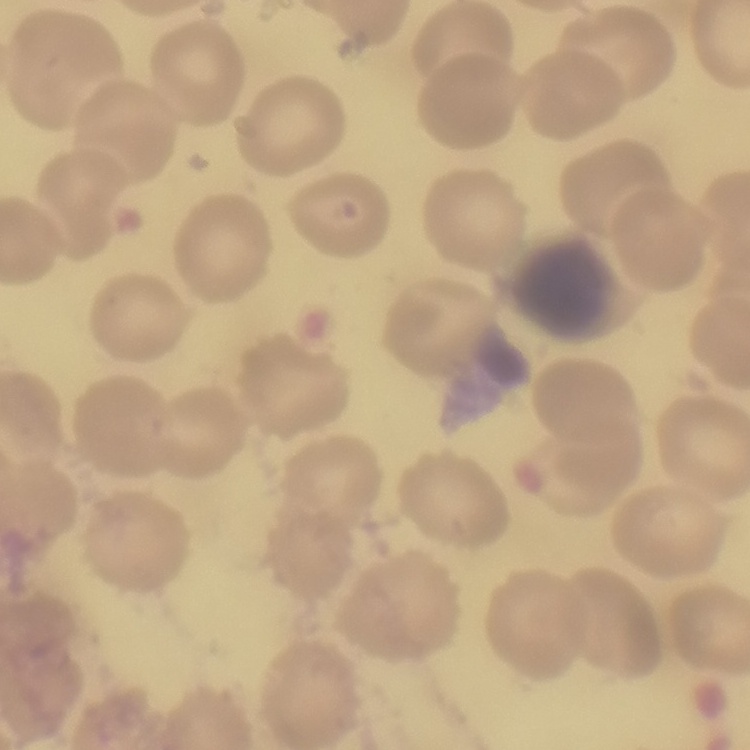

Summary:
  - Erythrocyte morphology: no rouleaux formation
  - Stain: Field's or Giemsa
  - Preparation: thin peripheral smear
  - Image type: square crop of a larger photomicrograph